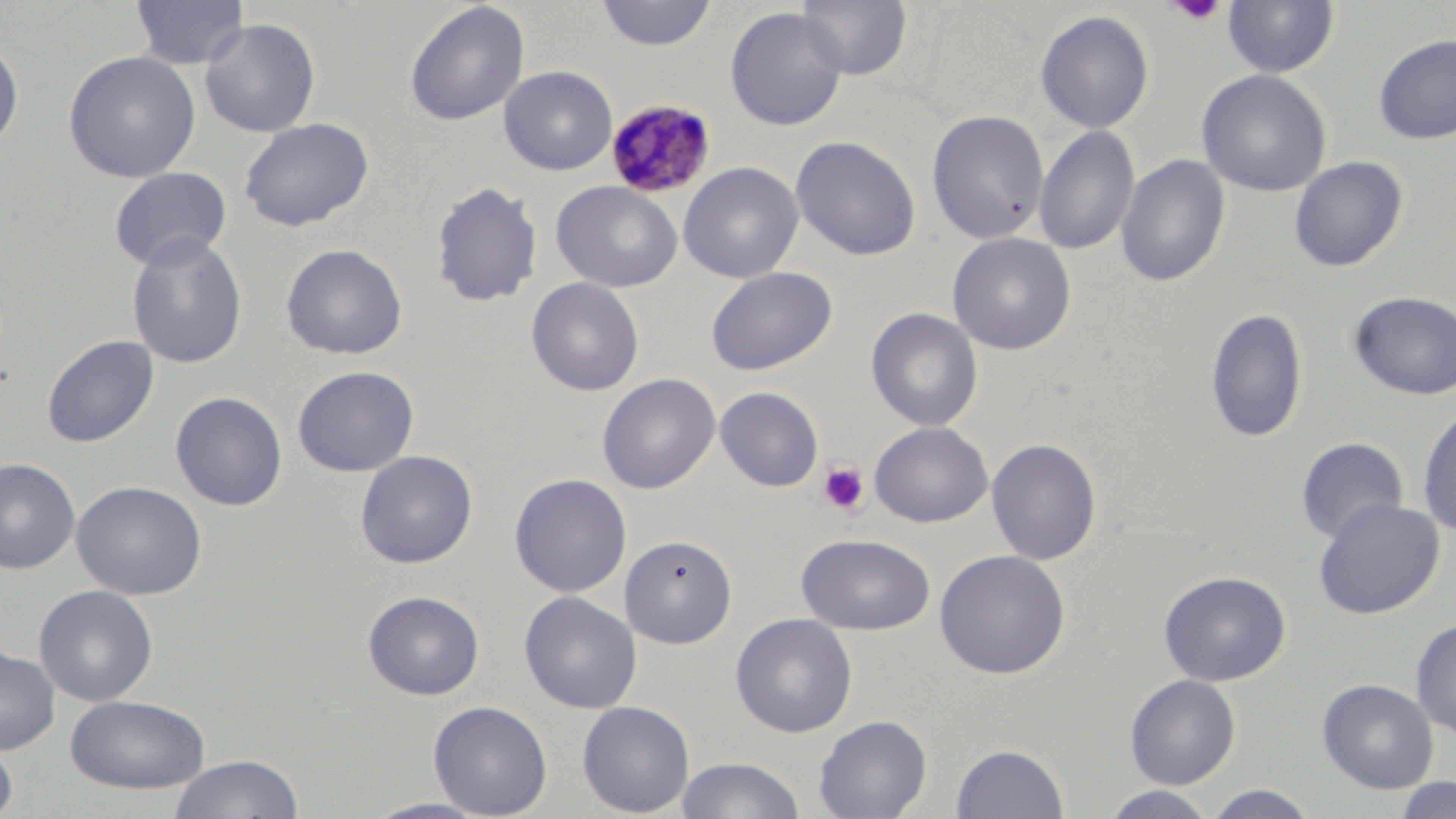

Summary:
  - Coordinate format: approximate bounding boxes as (x1,y1)-(x2,y2) corner pairs in pixels
  - Uninfected red blood cell locations: (130,0)-(249,70), (596,0)-(717,51), (796,0)-(912,80), (1221,1)-(1340,78), (405,2)-(529,126), (725,7)-(847,131), (1034,10)-(1155,134), (199,17)-(321,137), (1373,33)-(1456,144), (0,36)-(24,150), (62,50)-(200,183), (498,65)-(618,176), (1197,69)-(1332,198), (927,109)-(1049,245), (239,117)-(374,231), (1034,126)-(1139,255), (790,135)-(921,261), (1116,153)-(1231,289), (1288,155)-(1408,271), (678,161)-(803,283), (108,166)-(232,271), (431,180)-(543,308), (551,181)-(682,292), (433,183)-(675,303), (947,232)-(1076,355), (126,233)-(248,369), (281,243)-(408,359), (705,266)-(837,376), (526,277)-(644,396), (1349,290)-(1456,400), (865,307)-(983,432), (1205,307)-(1309,443), (41,335)-(158,448), (292,366)-(419,477), (596,373)-(720,495), (715,386)-(824,492), (170,391)-(288,511), (1417,403)-(1456,537), (869,421)-(993,528), (1295,437)-(1410,544), (986,438)-(1102,566), (355,450)-(478,569), (0,458)-(80,575), (509,473)-(632,598), (71,480)-(207,600), (1312,497)-(1445,619), (797,533)-(936,635), (620,534)-(737,648), (933,549)-(1071,679), (1158,570)-(1291,686), (33,585)-(158,706), (363,590)-(484,700), (519,591)-(641,714), (730,612)-(858,737), (1411,619)-(1456,737), (0,646)-(60,755), (1124,673)-(1241,788), (1317,678)-(1438,794), (64,694)-(211,794), (428,700)-(553,818), (577,700)-(695,816), (813,714)-(932,819), (0,738)-(17,819), (951,743)-(1069,818), (168,753)-(304,819), (675,756)-(805,818), (1392,776)-(1456,818), (1202,785)-(1320,819), (1101,786)-(1218,819), (361,797)-(495,818)
  - Plasmodium malariae-infected red blood cell locations: (606,99)-(718,198)
  - Platelet locations: (1167,1)-(1226,25), (818,462)-(870,515)
  - Slide-level diagnosis: Plasmodium malariae
  - Field of view: single
  - Image size: 1456×819 pixels
  - Modality: light microscopy
  - Magnification: 1000x
  - Stain: May-Grünwald-Giemsa
  - Preparation: thin blood film